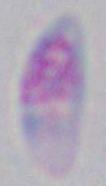 Toxoplasma gondii is shown. 1000x magnification. Micrograph.